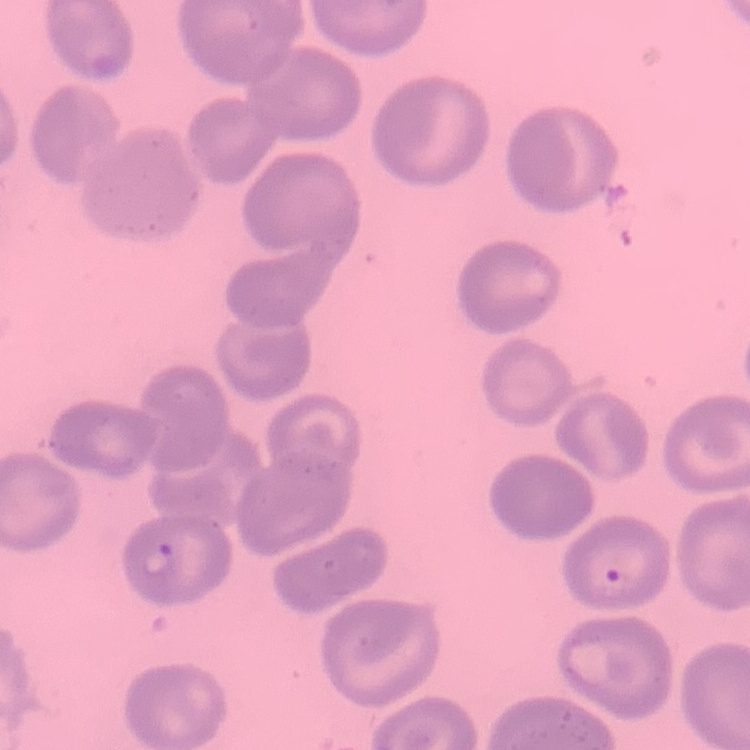
The red blood cells exhibit no rouleaux formation. Field's or Giemsa stain. Thin blood smear. Square crop of a larger photomicrograph.